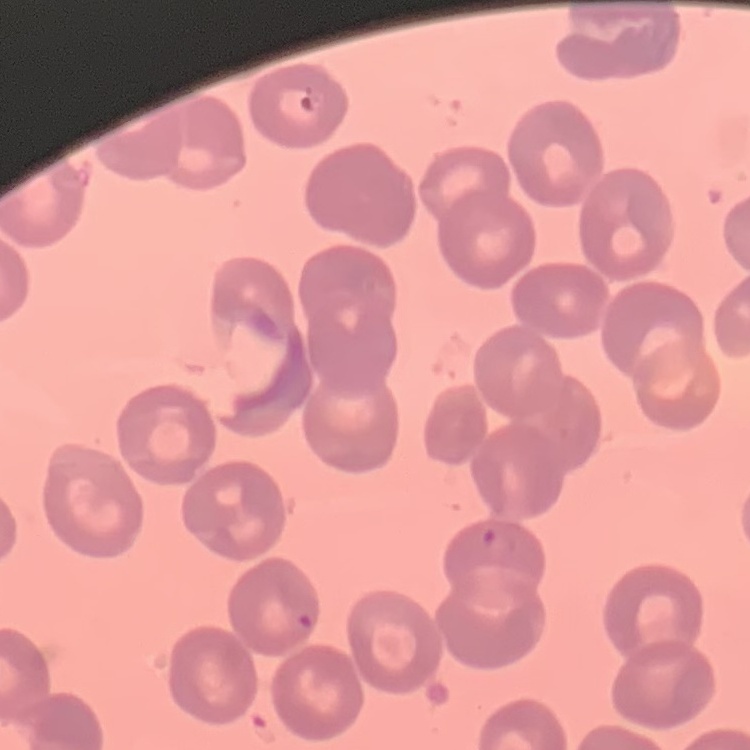
Summary:
  - Red blood cell morphology: no rouleaux formation
  - Preparation: thin blood smear
  - Image type: one tile cut from a larger photomicrograph
  - Stain: Field's or Giemsa